Identify the parasite.
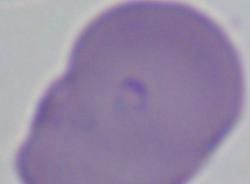
This is Babesia.

modality = photomicrograph
magnification = 1000x